Name the parasite shown.
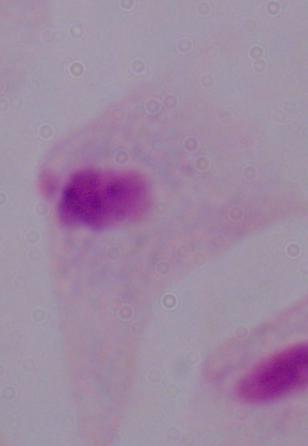
A trichomonad.

modality: photomicrograph
magnification: 1000x